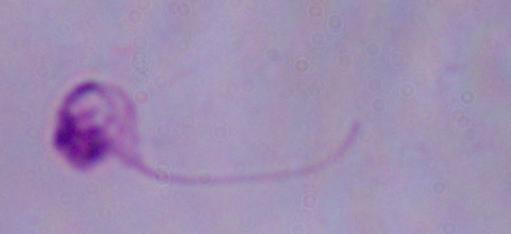

modality = micrograph
identification = Leishmania
magnification = 1000x